Identify the preparation type.
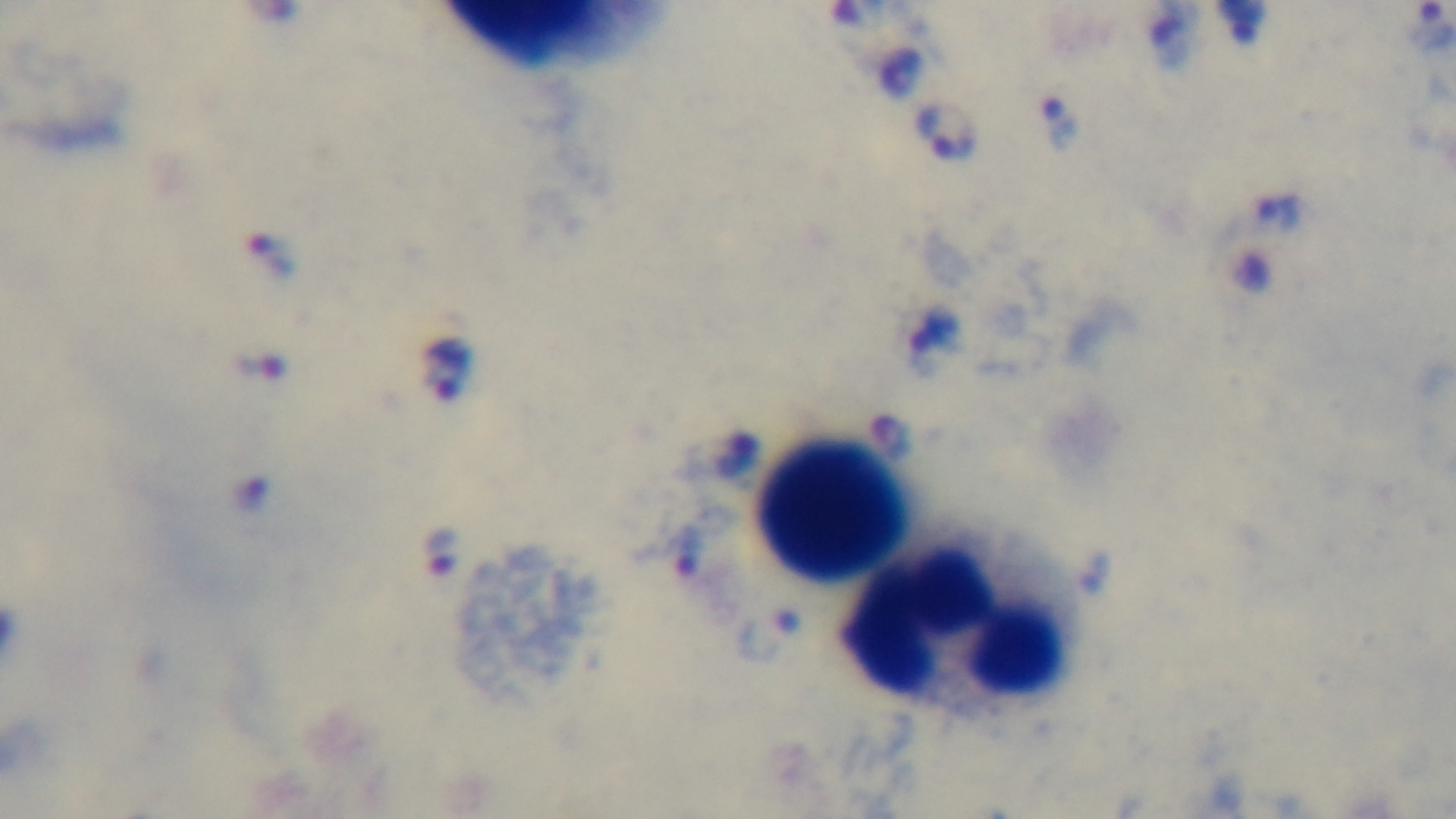

A thick smear.

stain = Giemsa
capture = mounted 4K digital camera
malaria status = infected
objective = 100x oil immersion
modality = light microscopy
field of view = single